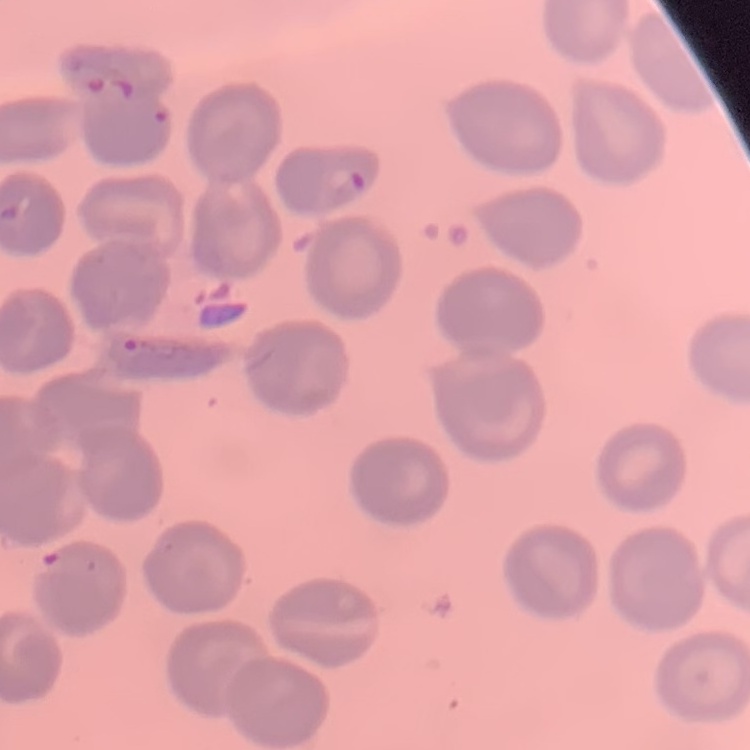
{
  "erythrocyte_morphology": "no rouleaux formation",
  "stain": "Field's or Giemsa",
  "image_type": "square crop of a larger photomicrograph",
  "preparation": "thin blood smear"
}